Report the malaria status of this cell.
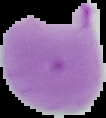
Parasitized.

Summary:
  - Image type: cell region segmented out of the field of view; surrounding area masked to black
  - Image size: 106×118 pixels
  - Preparation: thin blood smear